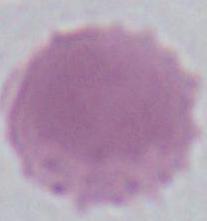

1000x magnification. An erythrocyte is seen. Photomicrograph.